Locate every uninfected red blood cell.
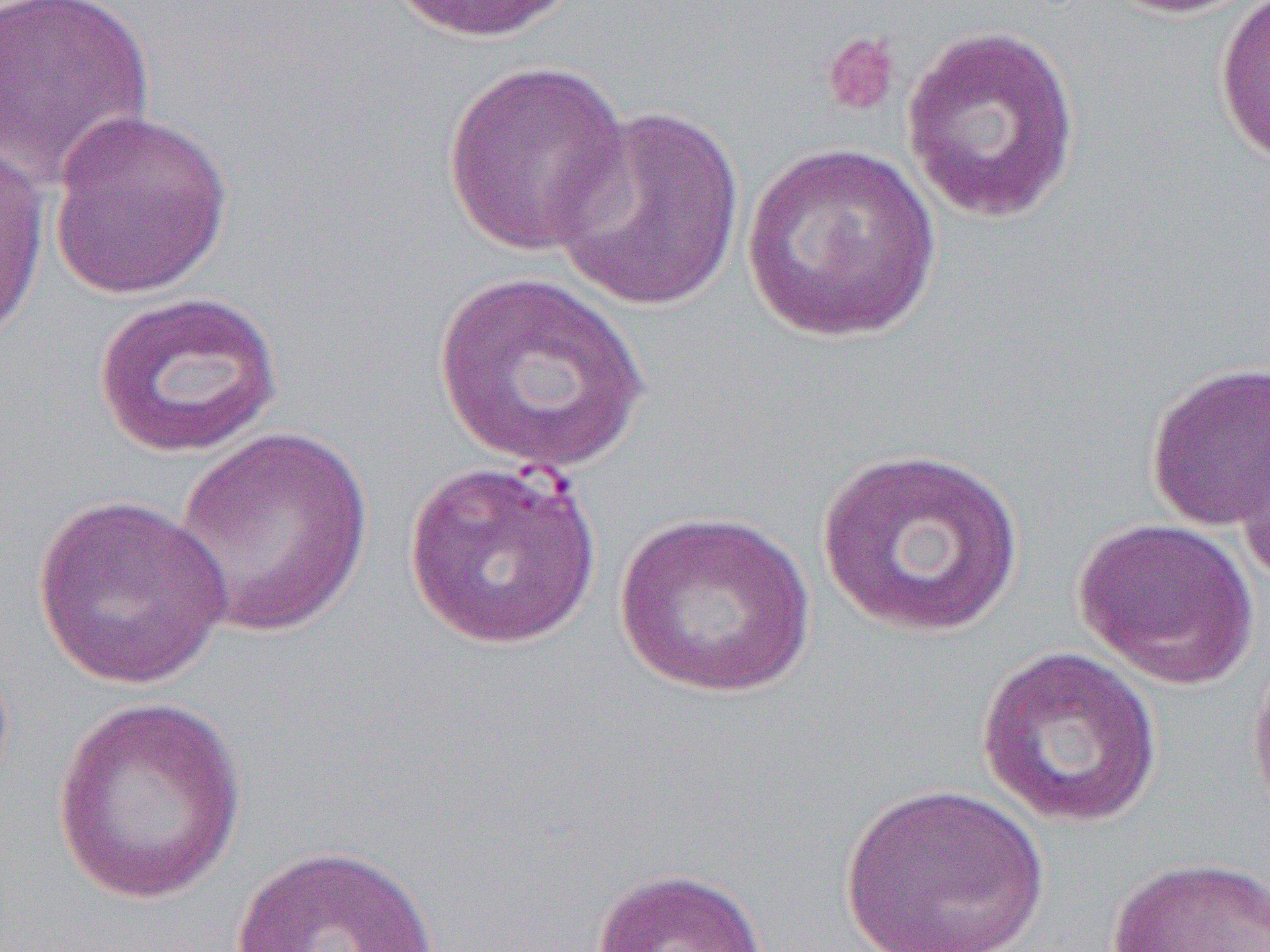

Approximate bounding boxes as [x1, y1, x2, y2] in pixels.
Uninfected red blood cells (subset): [0, 0, 157, 189], [385, 0, 585, 43], [1099, 0, 1264, 18], [1214, 1, 1270, 167], [900, 23, 1082, 223], [441, 58, 632, 257], [549, 103, 747, 312], [46, 106, 235, 300], [0, 138, 50, 349], [742, 143, 940, 343], [433, 269, 649, 474], [91, 291, 284, 459], [1144, 361, 1270, 531], [1233, 424, 1270, 584], [173, 426, 375, 638], [815, 446, 1027, 639], [404, 457, 601, 649], [32, 493, 236, 690], [616, 509, 817, 699], [1074, 516, 1260, 689], [975, 644, 1165, 830], [1248, 649, 1270, 828], [50, 697, 248, 906], [838, 782, 1051, 952], [226, 843, 446, 952], [1105, 855, 1269, 952], [589, 866, 772, 952].

Summary:
  - Slide-level diagnosis: Plasmodium falciparum
  - Modality: light microscopy
  - Magnification: 1000x
  - Image size: 1270×952 pixels
  - Preparation: thin blood film
  - Field of view: single